Report the malaria status of this cell.
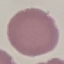
It is uninfected.

image type = cell patch, automatically extracted from a larger field of view and resized to 64 × 64 pixels
capture = smartphone through the microscope eyepiece
stain = Giemsa
preparation = thin smear